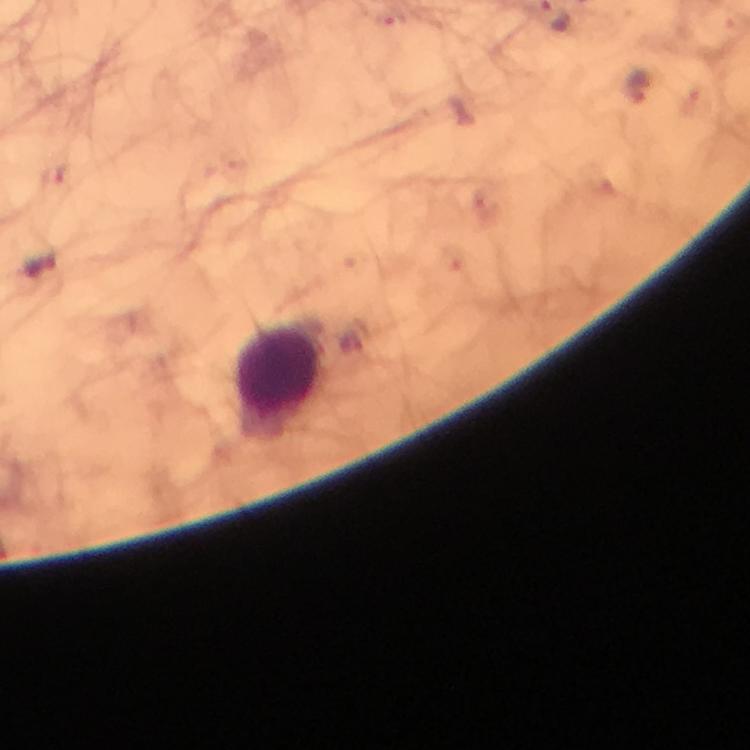
{
  "image_size": "750×750 pixels",
  "preparation": "thick blood film",
  "stain": "Giemsa",
  "leukocyte_locations": "approximate centers as {x, y} in pixels: {282, 370}",
  "magnification": "100x",
  "malaria_parasite_locations": "approximate centers as {x, y} in pixels: {639, 85}, {38, 266}, {354, 337}",
  "context": "from a malaria diagnostic workup",
  "immersion_oil": "used",
  "capture": "smartphone mounted on the microscope",
  "cropped_from": "a single field of view"
}